Assess the morphology of the red blood cells.
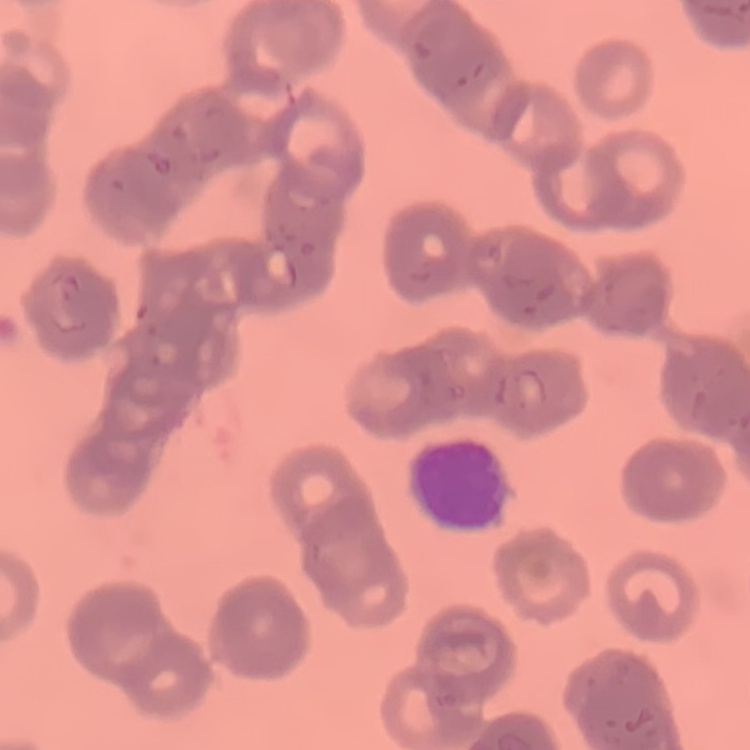

Rouleaux formation.

Summary:
  - Image type: one tile cut from a larger photomicrograph
  - Stain: Field's or Giemsa
  - Preparation: thin blood smear